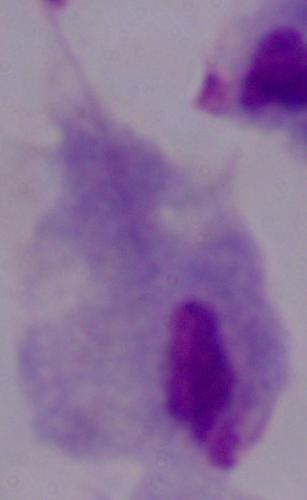
A trichomonad is seen. 1000x magnification. Micrograph.